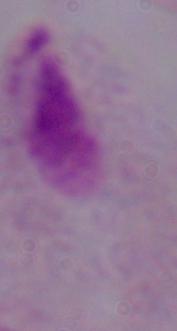
Summary:
  - Identification: trichomonad
  - Modality: micrograph
  - Magnification: 1000x